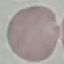

result = negative for malaria parasites
capture = smartphone camera at the microscope eyepiece
preparation = thin blood film
image type = cell patch, automatically extracted from a larger field of view and resized to 64 × 64 pixels
stain = Giemsa